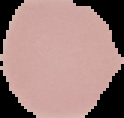
result = no Plasmodium parasites detected
image size = 124×118 pixels
image type = cell region segmented out of the field of view; surrounding area masked to black
preparation = thin blood film